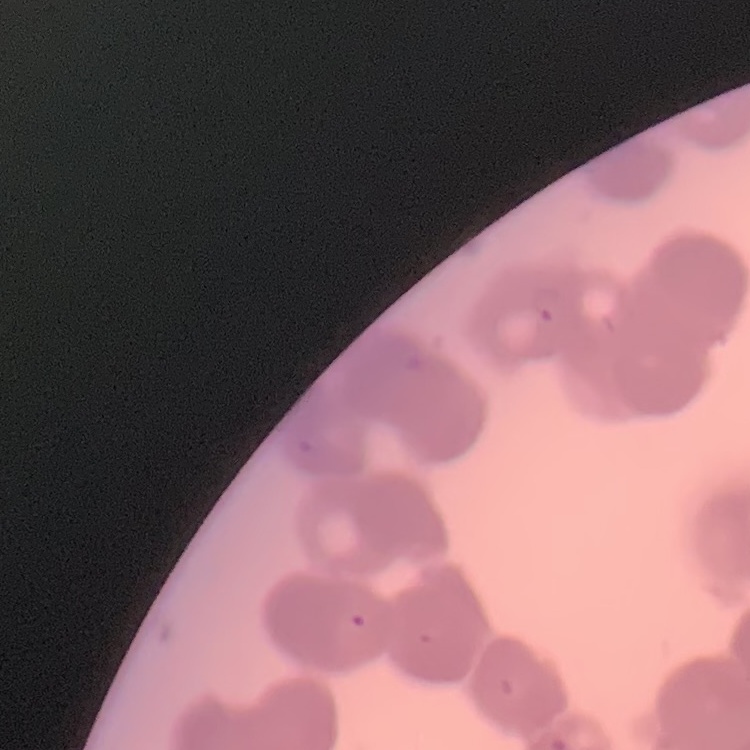
{
  "red_blood_cell_morphology": "rouleaux formation",
  "image_type": "one tile cut from a larger photomicrograph",
  "stain": "Field's or Giemsa",
  "preparation": "thin peripheral smear"
}